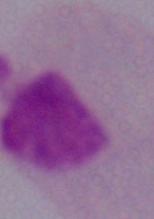

Summary:
  - Identification: trichomonad
  - Magnification: 1000x
  - Modality: photomicrograph